Name the parasite shown.
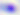
This is Toxoplasma gondii.

Captured at 400x magnification. Micrograph.